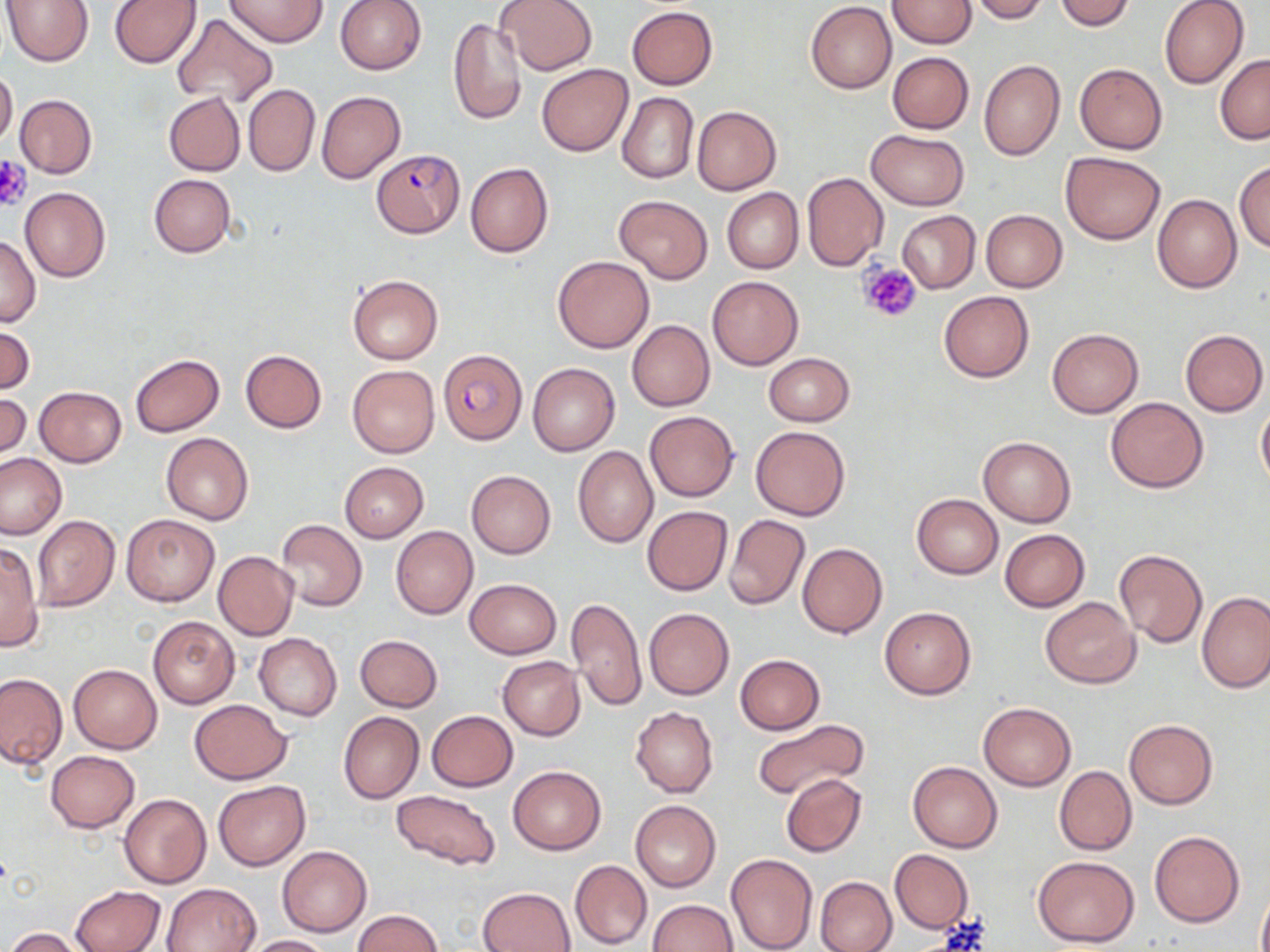
Summary:
  - Coordinate format: approximate bounding boxes as named x1/y1/x2/y2 corners in pixels
  - Platelet locations: (x1=0, y1=156, x2=32, y2=210), (x1=858, y1=261, x2=922, y2=323)
  - Uninfected red blood cell locations: (x1=3, y1=0, x2=95, y2=66), (x1=226, y1=0, x2=329, y2=47), (x1=335, y1=0, x2=426, y2=74), (x1=497, y1=0, x2=597, y2=75), (x1=888, y1=0, x2=976, y2=48), (x1=967, y1=0, x2=1048, y2=23), (x1=1054, y1=0, x2=1136, y2=31), (x1=1160, y1=0, x2=1248, y2=88), (x1=108, y1=1, x2=200, y2=69), (x1=806, y1=2, x2=897, y2=93), (x1=626, y1=6, x2=717, y2=90), (x1=171, y1=12, x2=277, y2=107), (x1=447, y1=17, x2=528, y2=126), (x1=887, y1=52, x2=974, y2=133), (x1=1215, y1=54, x2=1270, y2=144), (x1=979, y1=60, x2=1066, y2=161), (x1=1074, y1=63, x2=1168, y2=154), (x1=536, y1=64, x2=632, y2=156), (x1=0, y1=68, x2=18, y2=150), (x1=243, y1=83, x2=320, y2=177), (x1=317, y1=90, x2=405, y2=184), (x1=617, y1=91, x2=699, y2=184), (x1=163, y1=92, x2=245, y2=176), (x1=14, y1=94, x2=97, y2=178), (x1=691, y1=106, x2=781, y2=195), (x1=865, y1=129, x2=970, y2=210), (x1=1061, y1=151, x2=1165, y2=245), (x1=1234, y1=160, x2=1270, y2=252), (x1=465, y1=163, x2=553, y2=258), (x1=803, y1=172, x2=889, y2=270), (x1=149, y1=174, x2=235, y2=258), (x1=21, y1=187, x2=110, y2=282), (x1=722, y1=188, x2=803, y2=273), (x1=1152, y1=193, x2=1242, y2=293), (x1=613, y1=196, x2=714, y2=283), (x1=980, y1=209, x2=1067, y2=292), (x1=898, y1=211, x2=980, y2=292), (x1=0, y1=234, x2=41, y2=327), (x1=553, y1=255, x2=654, y2=353), (x1=347, y1=274, x2=443, y2=363), (x1=706, y1=274, x2=804, y2=370), (x1=938, y1=292, x2=1033, y2=382), (x1=627, y1=321, x2=714, y2=411), (x1=0, y1=325, x2=35, y2=396), (x1=1047, y1=329, x2=1143, y2=418), (x1=1179, y1=329, x2=1268, y2=416), (x1=240, y1=350, x2=327, y2=434), (x1=763, y1=352, x2=855, y2=426), (x1=131, y1=354, x2=225, y2=436), (x1=528, y1=363, x2=620, y2=455), (x1=347, y1=365, x2=440, y2=457), (x1=35, y1=386, x2=126, y2=467), (x1=0, y1=392, x2=30, y2=461), (x1=1107, y1=397, x2=1208, y2=492), (x1=1256, y1=400, x2=1270, y2=492), (x1=644, y1=411, x2=740, y2=502), (x1=750, y1=425, x2=851, y2=520), (x1=161, y1=432, x2=254, y2=524), (x1=977, y1=435, x2=1075, y2=527), (x1=572, y1=446, x2=657, y2=547), (x1=0, y1=452, x2=69, y2=540), (x1=340, y1=463, x2=429, y2=543), (x1=466, y1=469, x2=556, y2=559), (x1=912, y1=494, x2=1003, y2=578), (x1=642, y1=505, x2=733, y2=596), (x1=122, y1=514, x2=218, y2=605), (x1=724, y1=514, x2=810, y2=609), (x1=33, y1=515, x2=119, y2=611), (x1=276, y1=519, x2=367, y2=612), (x1=391, y1=526, x2=477, y2=619), (x1=1000, y1=529, x2=1090, y2=611), (x1=0, y1=541, x2=43, y2=653), (x1=797, y1=542, x2=887, y2=638), (x1=1114, y1=549, x2=1209, y2=647), (x1=213, y1=551, x2=298, y2=641), (x1=464, y1=579, x2=561, y2=659), (x1=1197, y1=592, x2=1269, y2=692), (x1=1039, y1=595, x2=1140, y2=688), (x1=567, y1=598, x2=647, y2=712), (x1=880, y1=607, x2=975, y2=699), (x1=644, y1=608, x2=734, y2=700), (x1=148, y1=616, x2=239, y2=707), (x1=253, y1=633, x2=341, y2=721), (x1=354, y1=634, x2=442, y2=711), (x1=736, y1=654, x2=825, y2=735), (x1=497, y1=656, x2=585, y2=739), (x1=69, y1=664, x2=162, y2=753), (x1=0, y1=673, x2=66, y2=770), (x1=189, y1=699, x2=293, y2=784), (x1=978, y1=702, x2=1076, y2=791), (x1=630, y1=706, x2=718, y2=797), (x1=426, y1=711, x2=519, y2=791), (x1=338, y1=712, x2=424, y2=804), (x1=752, y1=719, x2=869, y2=799), (x1=1124, y1=719, x2=1218, y2=809), (x1=45, y1=750, x2=139, y2=832), (x1=909, y1=761, x2=1002, y2=852), (x1=508, y1=765, x2=605, y2=854), (x1=1054, y1=765, x2=1137, y2=855), (x1=781, y1=773, x2=866, y2=857), (x1=212, y1=781, x2=311, y2=870), (x1=390, y1=789, x2=502, y2=871), (x1=118, y1=793, x2=210, y2=889), (x1=630, y1=800, x2=721, y2=891), (x1=1149, y1=830, x2=1245, y2=928), (x1=277, y1=846, x2=372, y2=937), (x1=890, y1=849, x2=973, y2=933), (x1=726, y1=854, x2=817, y2=952), (x1=1031, y1=855, x2=1140, y2=947), (x1=569, y1=860, x2=652, y2=949), (x1=815, y1=876, x2=897, y2=952), (x1=162, y1=882, x2=260, y2=951), (x1=71, y1=884, x2=165, y2=952), (x1=1257, y1=885, x2=1270, y2=952), (x1=479, y1=886, x2=575, y2=952), (x1=647, y1=900, x2=739, y2=952), (x1=352, y1=909, x2=444, y2=952), (x1=4, y1=927, x2=85, y2=952), (x1=244, y1=935, x2=333, y2=952)
  - Plasmodium falciparum-infected red blood cell locations: (x1=372, y1=149, x2=464, y2=238), (x1=438, y1=349, x2=526, y2=444)
  - Slide-level diagnosis: Plasmodium falciparum
  - Image size: 1270×952 pixels
  - Stain: May-Grünwald-Giemsa
  - Modality: light microscopy
  - Preparation: thin blood film
  - Magnification: 1000x
  - Field of view: one of a larger specimen